Outline each Plasmodium falciparum-infected red blood cell.
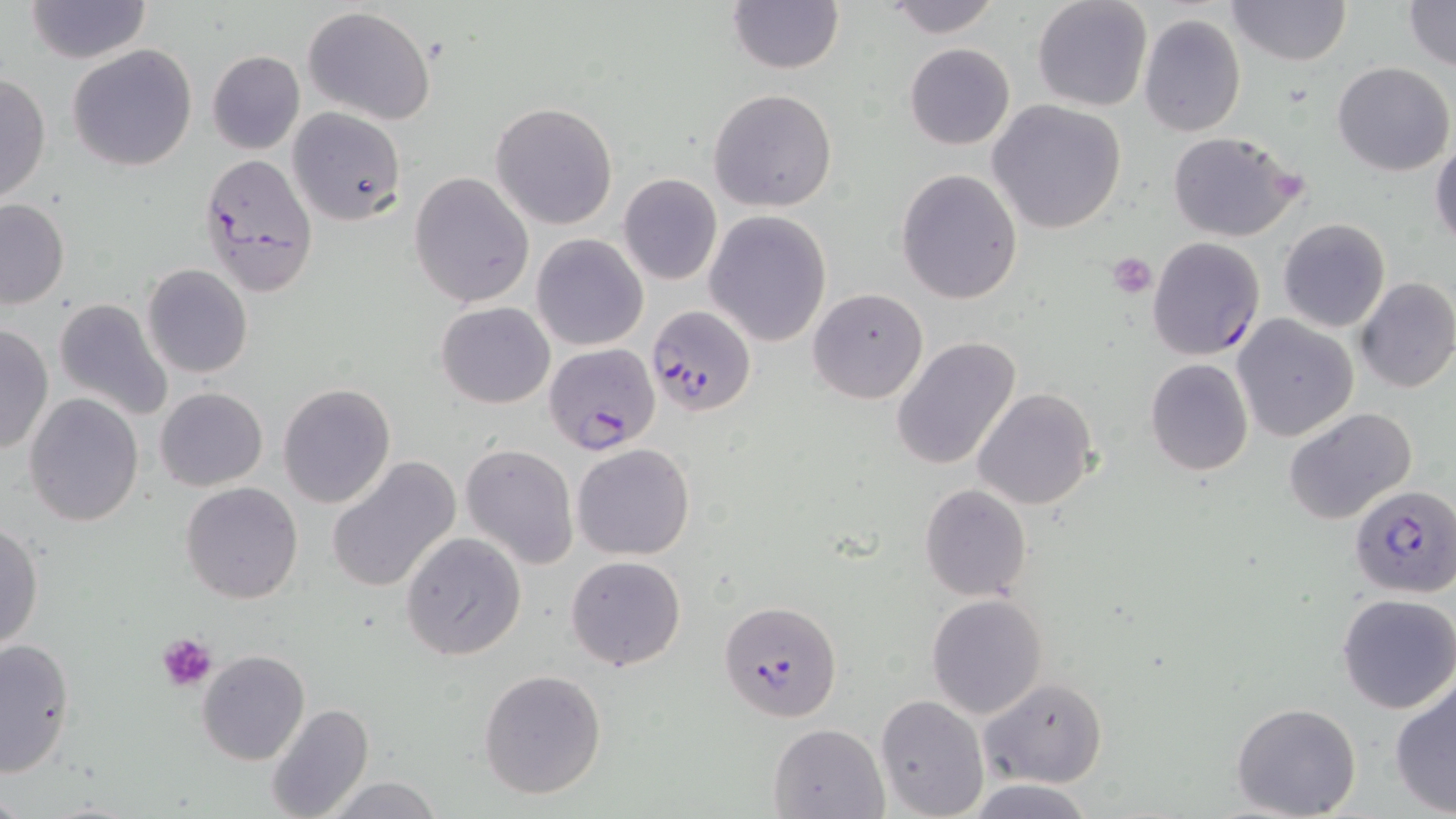

Approximate bounding boxes as [x1, y1, x2, y2] in pixels.
Plasmodium falciparum-infected red blood cells: [199, 151, 318, 295], [648, 302, 757, 417], [546, 344, 660, 456], [1351, 483, 1456, 596], [720, 600, 842, 721].

Platelet locations: [1107, 250, 1158, 296], [157, 631, 216, 692]. Uninfected red blood cell locations: [23, 0, 151, 63], [727, 0, 844, 74], [1032, 0, 1152, 113], [1225, 0, 1350, 67], [1404, 0, 1455, 71], [884, 1, 1002, 38], [301, 6, 436, 126], [1138, 14, 1246, 137], [904, 43, 1015, 150], [68, 45, 197, 172], [207, 50, 305, 154], [1332, 62, 1454, 177], [0, 71, 51, 207], [709, 89, 838, 212], [989, 100, 1128, 233], [490, 101, 618, 231], [286, 108, 404, 224], [1166, 131, 1306, 243], [1431, 132, 1456, 249], [896, 168, 1022, 305], [408, 170, 533, 308], [618, 173, 722, 286], [0, 197, 68, 309], [705, 210, 833, 347], [1278, 218, 1390, 332], [532, 234, 649, 351], [1145, 236, 1266, 360], [142, 263, 254, 378], [79, 265, 221, 413], [1354, 277, 1456, 393], [807, 286, 929, 405], [52, 296, 173, 424], [435, 302, 555, 409], [1232, 314, 1359, 442], [0, 325, 54, 456], [891, 337, 1023, 470], [1144, 358, 1253, 475], [278, 382, 397, 508], [156, 386, 268, 491], [973, 388, 1100, 509], [24, 394, 144, 526], [1283, 406, 1417, 524], [460, 443, 580, 569], [571, 443, 695, 560], [325, 456, 463, 595], [180, 481, 303, 603], [920, 483, 1033, 601], [0, 521, 43, 652], [399, 531, 527, 662], [565, 555, 687, 672], [1336, 594, 1456, 714], [926, 595, 1048, 719], [1, 638, 76, 777], [197, 650, 310, 765], [477, 668, 607, 800], [1388, 676, 1456, 818], [978, 677, 1108, 789], [876, 693, 989, 819], [1229, 701, 1362, 818], [266, 702, 374, 819], [768, 722, 890, 817], [321, 775, 445, 818], [964, 779, 1098, 817]. Slide-level diagnosis: Plasmodium falciparum. Thin blood smear. Image is 1456×819 pixels. Single field of view. May-Grünwald-Giemsa stain. Optical microscopy. Captured at 1000x magnification.